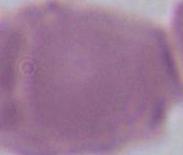
Summary:
  - Magnification: 1000x
  - Identification: red blood cell
  - Modality: micrograph